Assess the morphology of the red blood cells.
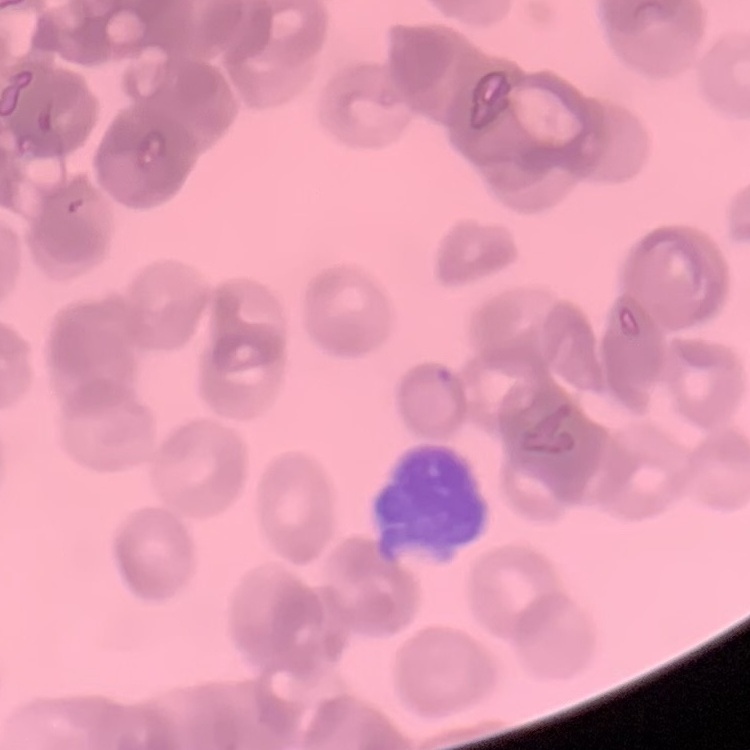

Rouleaux formation.

Summary:
  - Stain: Field's or Giemsa
  - Image type: one tile cut from a larger photomicrograph
  - Preparation: thin blood film